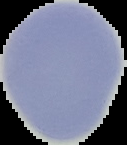
Summary:
  - Preparation: thin blood smear
  - Result: negative for malaria parasites
  - Image type: segmented cell region with the area outside set to black
  - Image size: 127×145 pixels